Classify the preparation.
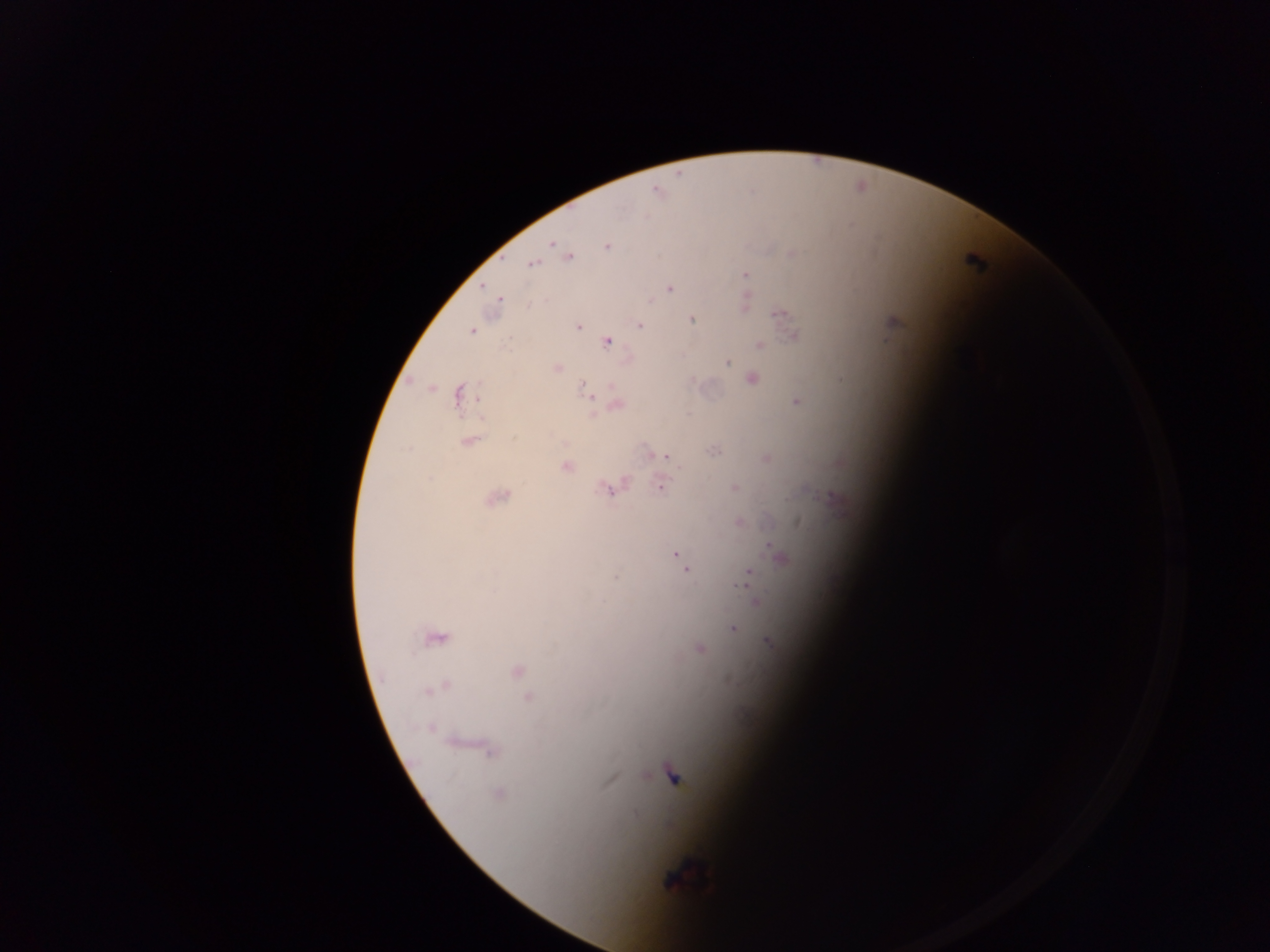

Thick blood film.

Approximate centers as x y in pixels. Malaria parasite locations: 656 191; 551 243; 607 246; 562 249; 791 254; 568 257; 532 264; 745 274; 669 289; 744 302; 496 304; 778 313; 691 319; 892 322; 576 326; 640 326; 471 331; 793 335; 606 341; 758 344; 725 361; 556 368; 751 379; 586 390; 460 394; 797 401; 615 404; 468 440; 714 451; 658 454; 666 456; 766 459; 660 463; 566 466; 661 484; 734 487; 610 488; 495 497; 834 499; 739 523; 768 544; 675 554; 782 557; 681 560; 685 568; 615 576; 745 579; 756 600; 733 628; 435 636; 768 641; 699 648; 516 670; 436 687; 527 697; 473 746; 487 749; 672 776; 497 794; 682 878. Single field of view. Image is 1270×952 pixels. Photographed through a microscope with a mobile-phone camera. Collected in Ghana.